Locate every Plasmodium parasite.
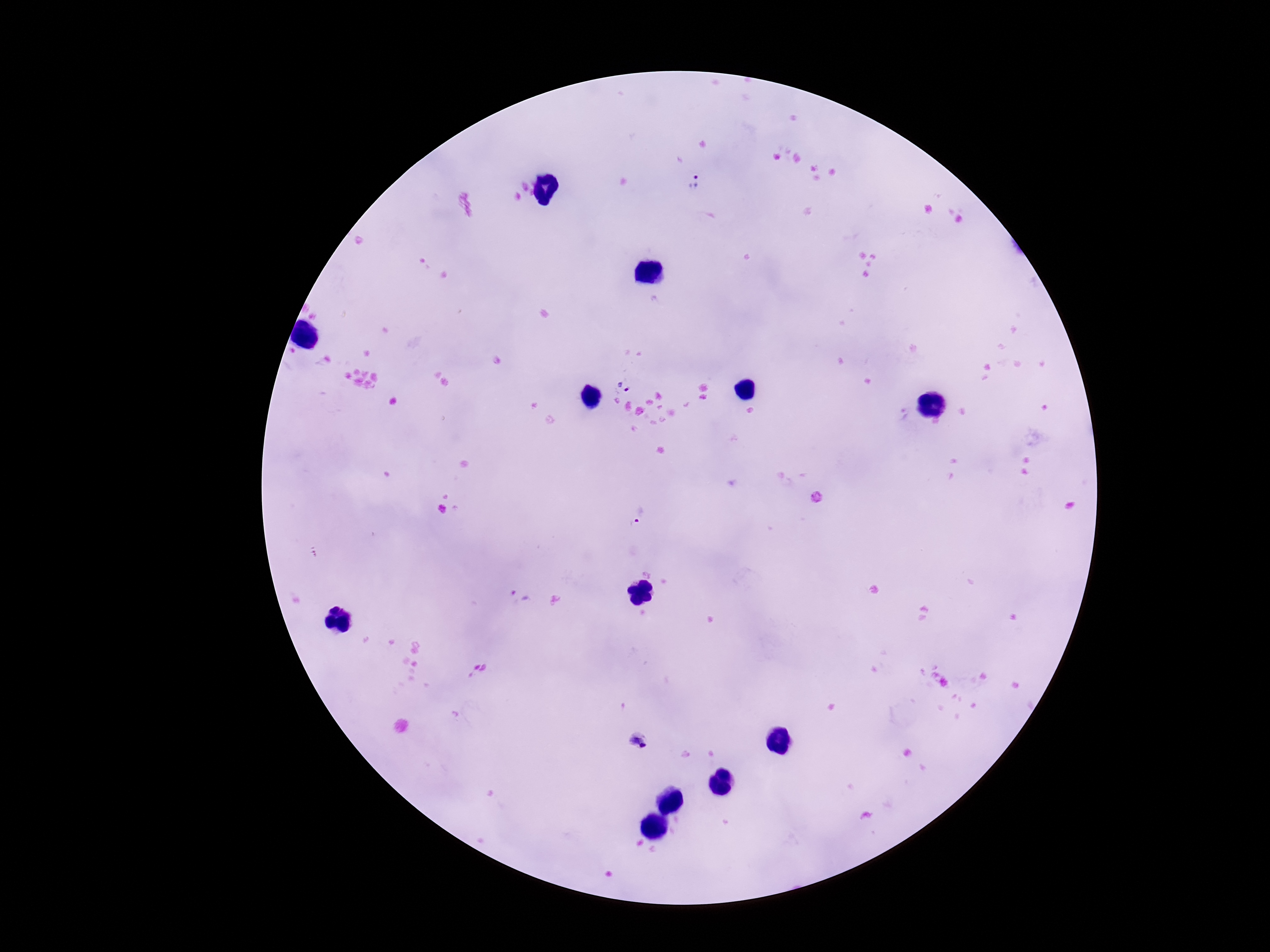

Approximate centers as (x, y) in pixels.
Plasmodium parasites: (696, 182), (623, 384), (904, 414), (636, 513), (639, 742).

One field from this slide. Image is 1270×952 pixels. Patient malaria status: infected. Smartphone photograph taken through the microscope eyepiece. 100x magnification. Thick blood film. Giemsa-stained preparation.